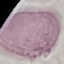
Summary:
  - Result: no malaria parasites seen
  - Capture: smartphone camera at the microscope eyepiece
  - Stain: Giemsa
  - Preparation: thin smear
  - Image type: cell patch, automatically extracted from a larger field of view and resized to 64 × 64 pixels